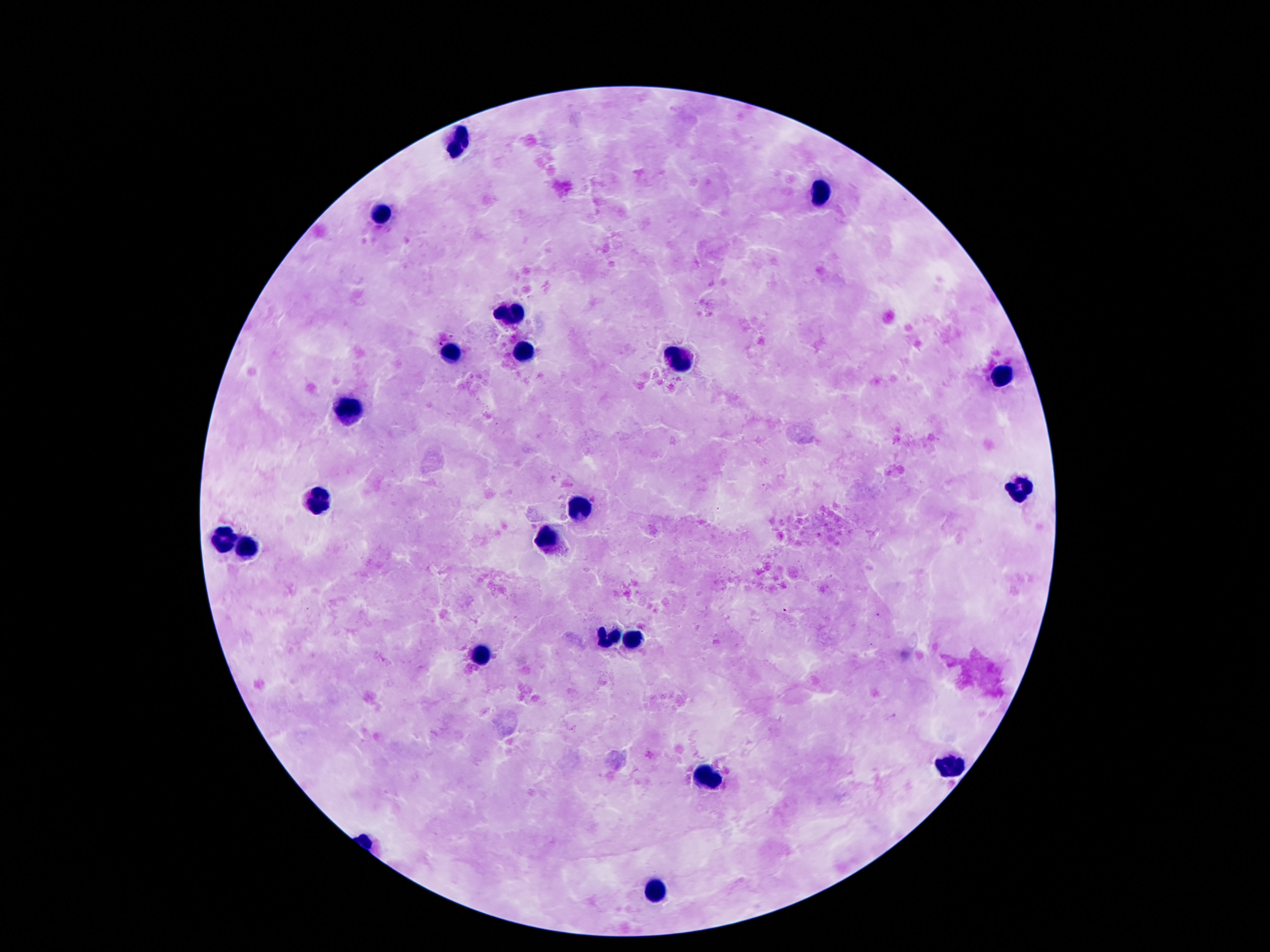
stain: Giemsa
capture: smartphone camera through the microscope eyepiece
magnification: 100x
image_size: 1270×952 pixels
leukocyte_locations: 'approximate centers as [x, y] in pixels: [460, 145], [820, 192], [386, 212], [509, 314], [525, 353], [451, 356], [679, 360], [1000, 376], [347, 413], [1019, 493], [320, 501], [578, 507], [550, 539], [220, 540], [247, 550], [605, 638], [638, 640], [478, 656], [951, 763], [708, 778], [656, 892]'
preparation: thick blood film
patient_malaria_status: negative
field_of_view: single